Point out every Plasmodium parasite.
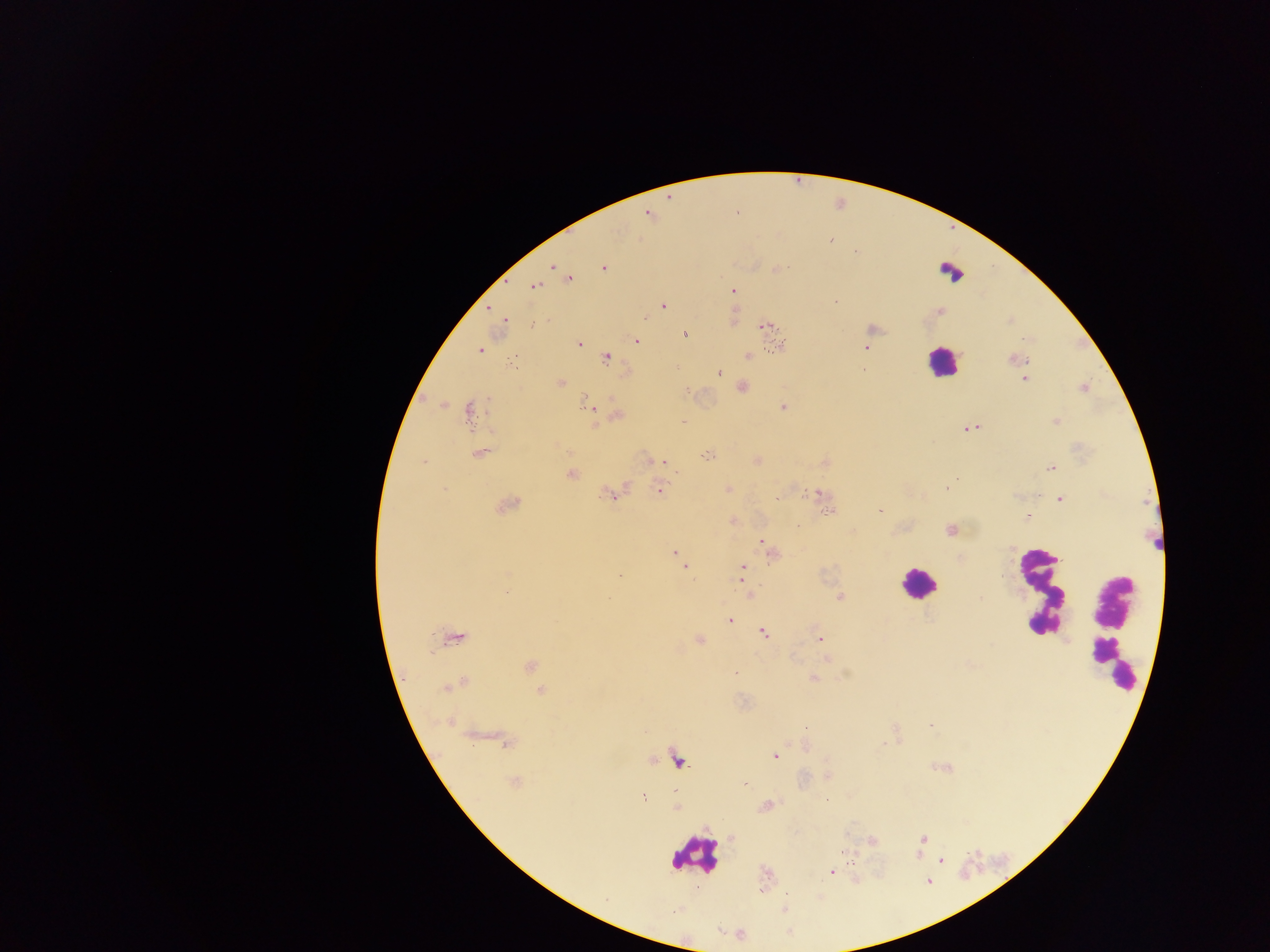

Approximate centers as x y in pixels.
Plasmodium parasites: 830 239; 856 252; 551 267; 603 268; 776 269; 570 278; 535 287; 733 292; 835 302; 663 306; 504 319; 764 326; 685 334; 637 341; 579 343; 779 346; 867 348; 479 350; 748 357; 606 358; 1016 359; 513 362; 718 373; 1024 379; 560 382; 743 387; 1084 388; 588 405; 783 407; 469 411; 618 414; 1057 421; 683 422; 967 428; 479 453; 708 455; 758 460; 423 461; 665 463; 1050 468; 571 475; 948 486; 443 489; 727 489; 660 491; 819 492; 612 494; 777 498; 1060 499; 507 505; 880 510; 829 512; 1027 516; 951 530; 761 540; 675 554; 683 565; 742 568; 619 577; 741 581; 506 592; 749 594; 840 597; 730 620; 763 633; 453 638; 699 640; 820 640; 827 659; 530 667; 735 674; 813 679; 454 685; 540 691; 931 725; 806 728; 503 742; 775 756; 513 782; 744 785; 643 798; 922 839; 873 841; 842 851; 941 860; 831 872; 928 882.

Summary:
  - Leukocyte locations: 947 273; 942 362; 917 584; 1042 592; 1112 627; 695 855
  - Image size: 1270×952 pixels
  - Preparation: thick blood film
  - Country: Ghana
  - Capture: mobile-phone photograph through a microscope
  - Field of view: single